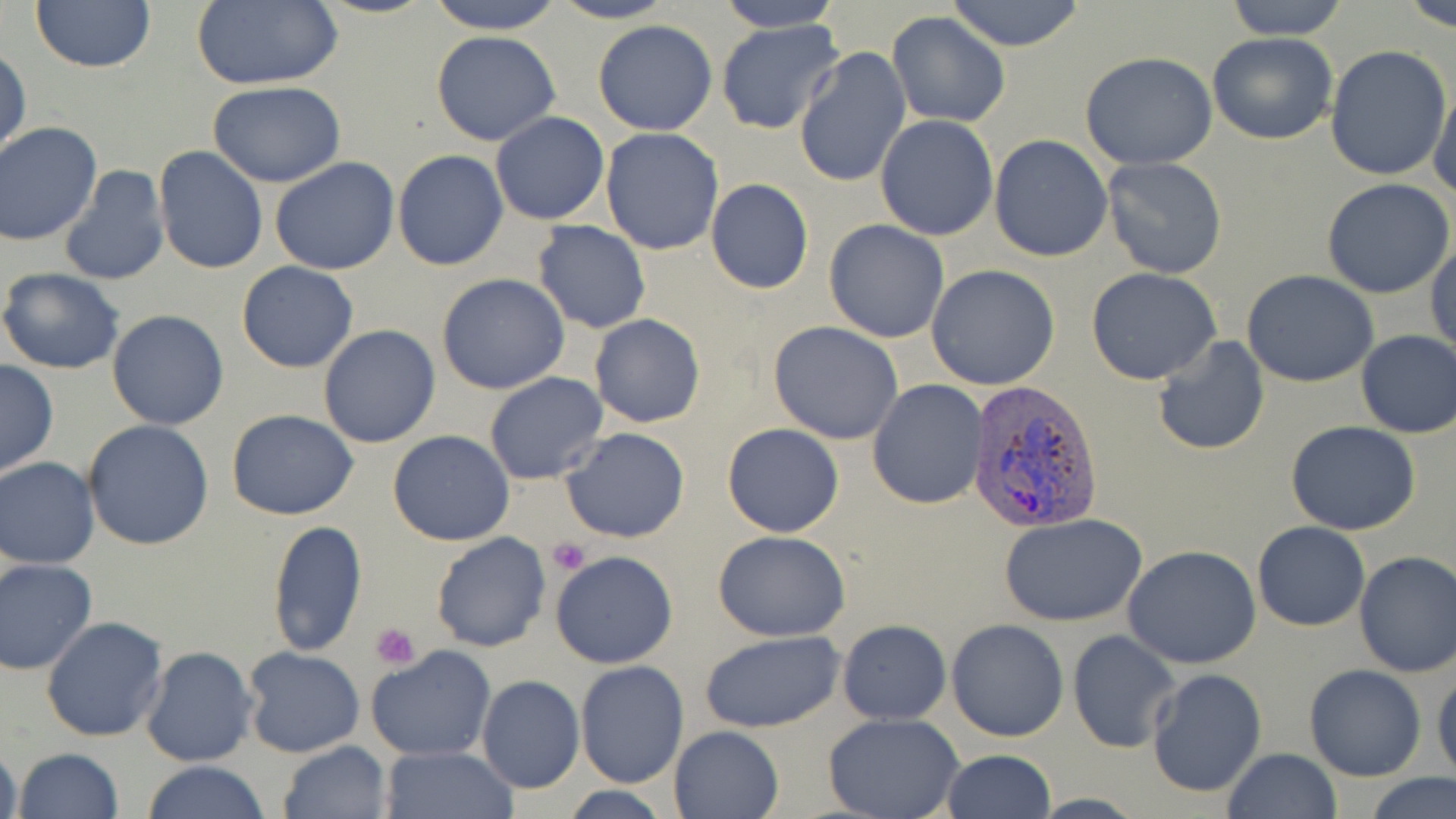
Summary:
  - Coordinate format: approximate bounding boxes as [x1, y1, x2, y2] in pixels
  - Platelet locations: [549, 538, 590, 576], [371, 622, 420, 670]
  - Uninfected red blood cell locations: [422, 0, 569, 34], [550, 0, 677, 24], [711, 0, 844, 33], [944, 0, 1087, 50], [1223, 0, 1351, 39], [1396, 0, 1456, 29], [30, 1, 157, 72], [189, 1, 342, 89], [886, 11, 1012, 128], [715, 19, 844, 135], [591, 20, 720, 136], [432, 31, 560, 145], [1208, 31, 1339, 145], [1324, 45, 1453, 180], [1, 46, 30, 163], [795, 47, 912, 188], [1080, 53, 1218, 169], [207, 80, 347, 186], [1428, 83, 1455, 202], [490, 112, 609, 225], [876, 115, 1000, 240], [0, 122, 103, 245], [600, 128, 726, 255], [988, 134, 1114, 262], [153, 146, 269, 276], [391, 150, 509, 270], [1101, 157, 1228, 280], [269, 158, 399, 276], [59, 164, 171, 288], [704, 178, 815, 294], [1321, 179, 1455, 298], [824, 219, 948, 342], [532, 220, 652, 333], [1428, 236, 1456, 359], [236, 261, 359, 373], [926, 264, 1059, 390], [1086, 267, 1221, 385], [0, 268, 126, 374], [1241, 271, 1380, 388], [436, 273, 569, 394], [106, 309, 230, 430], [590, 314, 706, 428], [768, 321, 905, 445], [318, 325, 441, 448], [1356, 329, 1456, 440], [1150, 335, 1271, 456], [0, 360, 58, 478], [484, 372, 608, 485], [867, 380, 987, 510], [225, 408, 359, 521], [82, 420, 215, 552], [1285, 420, 1422, 535], [722, 422, 844, 537], [560, 426, 691, 543], [387, 430, 515, 546], [1, 457, 100, 569], [998, 512, 1148, 627], [266, 518, 368, 656], [1252, 521, 1370, 632], [712, 530, 852, 642], [430, 531, 552, 652], [1123, 544, 1262, 668], [1352, 550, 1456, 676], [549, 552, 677, 669], [0, 557, 99, 676], [40, 616, 168, 742], [837, 619, 951, 724], [946, 619, 1069, 740], [1067, 629, 1180, 753], [699, 630, 847, 731], [141, 646, 258, 766], [365, 646, 497, 763], [241, 647, 365, 759], [575, 661, 689, 788], [1305, 664, 1427, 782], [1147, 668, 1266, 797], [1431, 669, 1456, 784], [477, 675, 584, 794], [823, 714, 965, 819], [668, 725, 784, 818], [1, 740, 25, 819], [279, 740, 392, 819], [382, 746, 516, 819], [13, 747, 124, 819], [1223, 747, 1343, 819], [940, 749, 1055, 819], [140, 760, 270, 819], [1367, 774, 1456, 819]
  - Plasmodium vivax-infected red blood cell locations: [967, 382, 1102, 536]
  - Slide-level diagnosis: Plasmodium vivax
  - Image size: 1456×819 pixels
  - Modality: optical microscopy
  - Field of view: single
  - Magnification: 1000x
  - Stain: May-Grünwald-Giemsa
  - Preparation: thin blood film